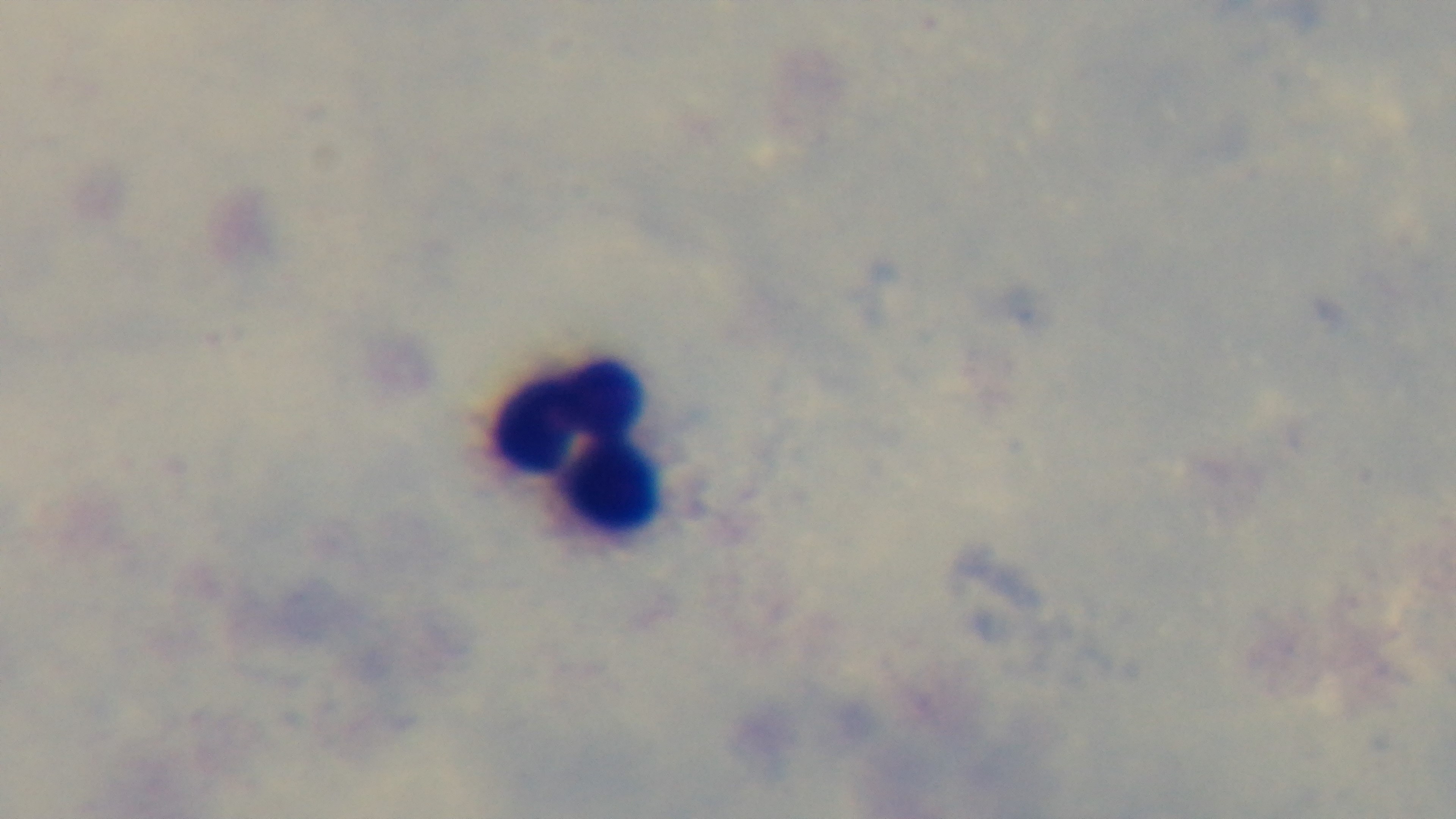
Captured with a mounted 4K digital camera. Light microscopy. Giemsa-stained. Preparation: thick blood film. One field from the slide. Oil-immersion objective, 100x. Malaria status: negative.